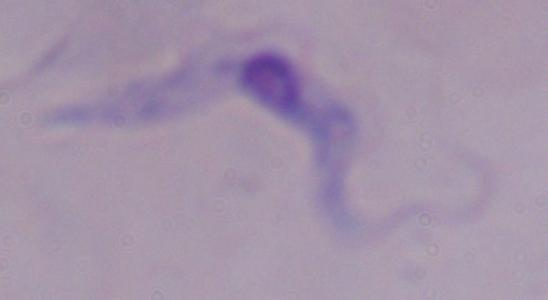
Captured at 1000x magnification. Photomicrograph. A trypanosome is seen.